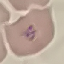

Summary:
  - Malaria status: parasitized
  - Image type: automatically extracted cell patch, resized to 64 × 64 pixels
  - Preparation: thin blood smear
  - Stain: Giemsa
  - Capture: smartphone camera at the microscope eyepiece